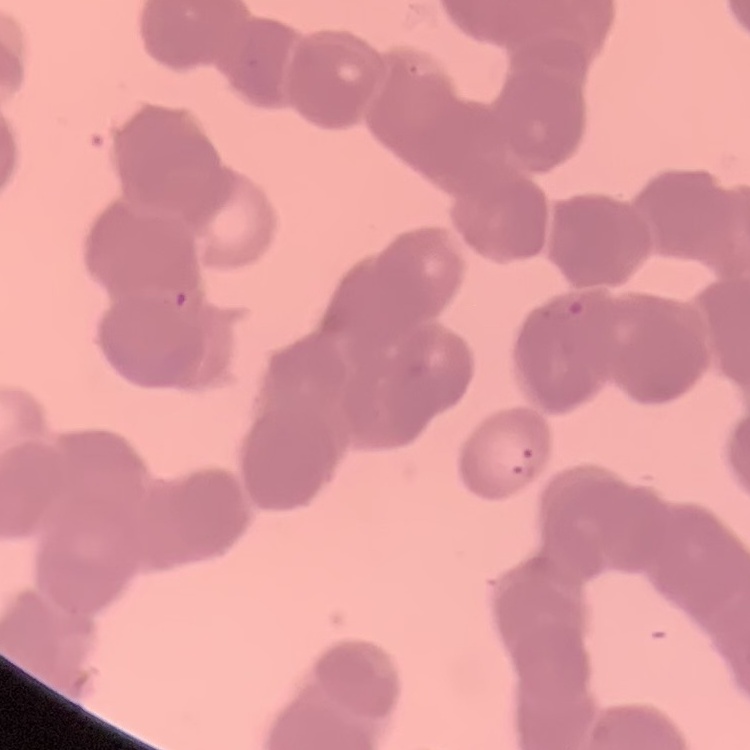

Summary:
  - Erythrocyte morphology: rouleaux formation
  - Stain: Field's or Giemsa
  - Image type: one tile cut from a larger photomicrograph
  - Preparation: thin peripheral smear